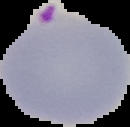
Summary:
  - Malaria status: parasitized
  - Image size: 130×127 pixels
  - Image type: cell region segmented out of the field of view; surrounding area masked to black
  - Preparation: thin blood film